Assess this cell for malaria.
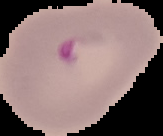

Parasitized.

Summary:
  - Image type: segmented cell region with the area outside set to black
  - Image size: 163×136 pixels
  - Preparation: thin blood film